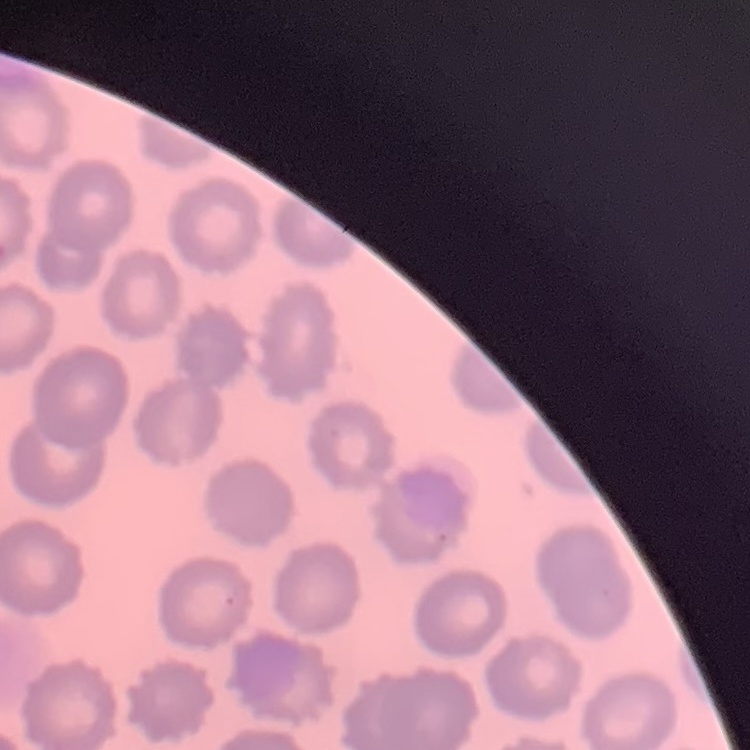

Summary:
  - Red blood cell morphology: no rouleaux formation
  - Stain: Field's or Giemsa
  - Image type: square crop of a larger photomicrograph
  - Preparation: thin blood film